Classify this cell by malaria status.
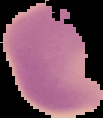
It is uninfected.

{
  "image_type": "segmented cell region with the area outside set to black",
  "preparation": "thin blood smear",
  "image_size": "103×118 pixels"
}